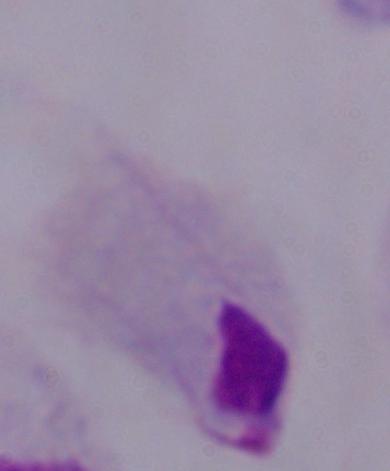

magnification = 1000x
modality = photomicrograph
identification = trichomonad